Assess the morphology of the erythrocytes.
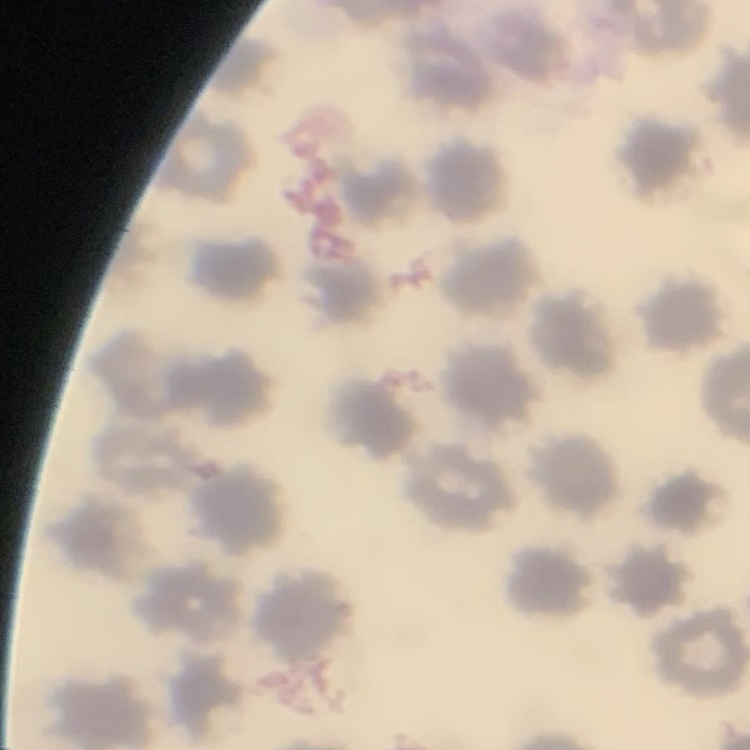

No rouleaux formation.

Thin blood smear. Field's or Giemsa stain. One tile cut from a larger photomicrograph.